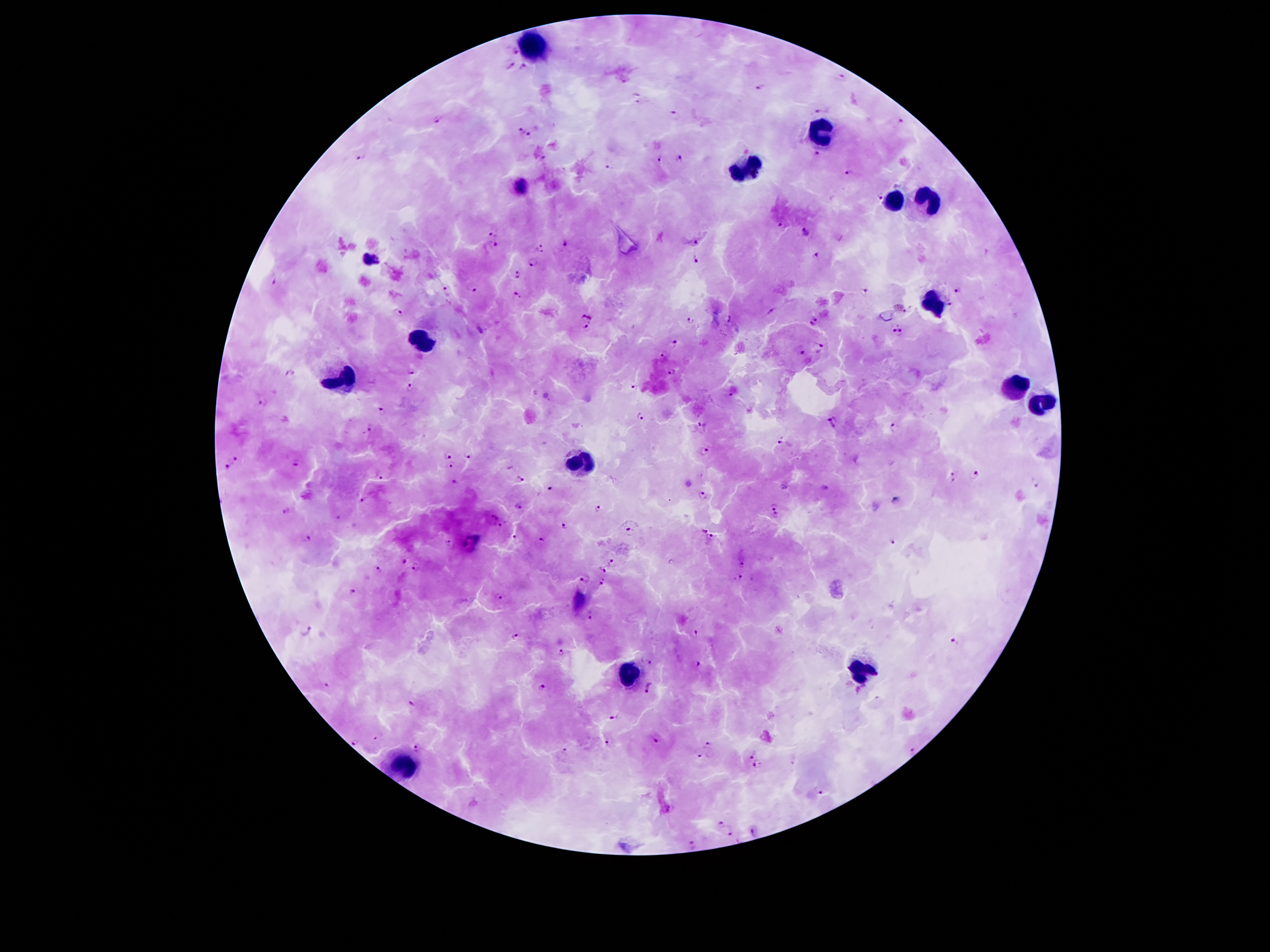

Approximate centers as [x, y] in pixels. Malaria parasite locations: [514, 49], [511, 65], [526, 66], [842, 76], [759, 88], [638, 98], [817, 110], [675, 115], [438, 119], [900, 122], [519, 127], [529, 133], [816, 153], [361, 157], [679, 158], [660, 159], [610, 166], [848, 172], [521, 188], [879, 196], [781, 225], [806, 230], [493, 232], [696, 239], [567, 243], [491, 245], [540, 248], [817, 252], [370, 258], [695, 258], [533, 263], [516, 273], [275, 279], [473, 288], [446, 290], [863, 290], [957, 290], [515, 297], [950, 305], [397, 311], [772, 311], [588, 315], [690, 318], [729, 319], [814, 321], [586, 326], [898, 333], [675, 343], [819, 344], [801, 351], [665, 355], [411, 370], [290, 371], [673, 371], [410, 385], [635, 387], [731, 393], [262, 400], [382, 411], [640, 418], [833, 420], [703, 425], [894, 426], [369, 431], [782, 440], [704, 447], [448, 453], [470, 455], [235, 459], [298, 461], [449, 464], [228, 468], [509, 468], [974, 473], [380, 476], [519, 478], [953, 478], [455, 482], [1036, 483], [550, 487], [702, 495], [362, 499], [896, 499], [773, 505], [518, 506], [597, 509], [288, 510], [339, 515], [492, 516], [775, 517], [502, 525], [565, 525], [631, 529], [704, 529], [711, 537], [306, 538], [514, 539], [544, 539], [893, 540], [450, 541], [404, 559], [612, 561], [740, 565], [379, 567], [416, 567], [603, 569], [742, 578], [584, 579], [602, 582], [350, 590], [499, 597], [591, 617], [306, 631], [696, 631], [515, 635], [955, 642], [561, 652], [645, 658], [695, 665], [325, 684], [543, 687], [649, 688], [413, 702], [613, 716], [376, 737], [658, 738], [354, 743], [607, 743], [709, 744], [417, 748], [913, 749], [564, 754], [752, 754], [700, 756], [758, 764], [819, 791], [721, 825], [757, 831], [730, 832], [691, 843]. Leukocyte locations: [531, 50], [823, 129], [748, 169], [926, 201], [895, 203], [937, 304], [420, 341], [342, 381], [1014, 388], [1040, 404], [580, 459], [861, 673], [628, 675], [405, 765]. Patient malaria status: positive for Plasmodium falciparum. Image is 1270×952 pixels. 100x magnification. One field from this slide. Photographed through the microscope eyepiece with a smartphone camera. Thick blood film. Giemsa-stained preparation.